Point out each Plasmodium parasite.
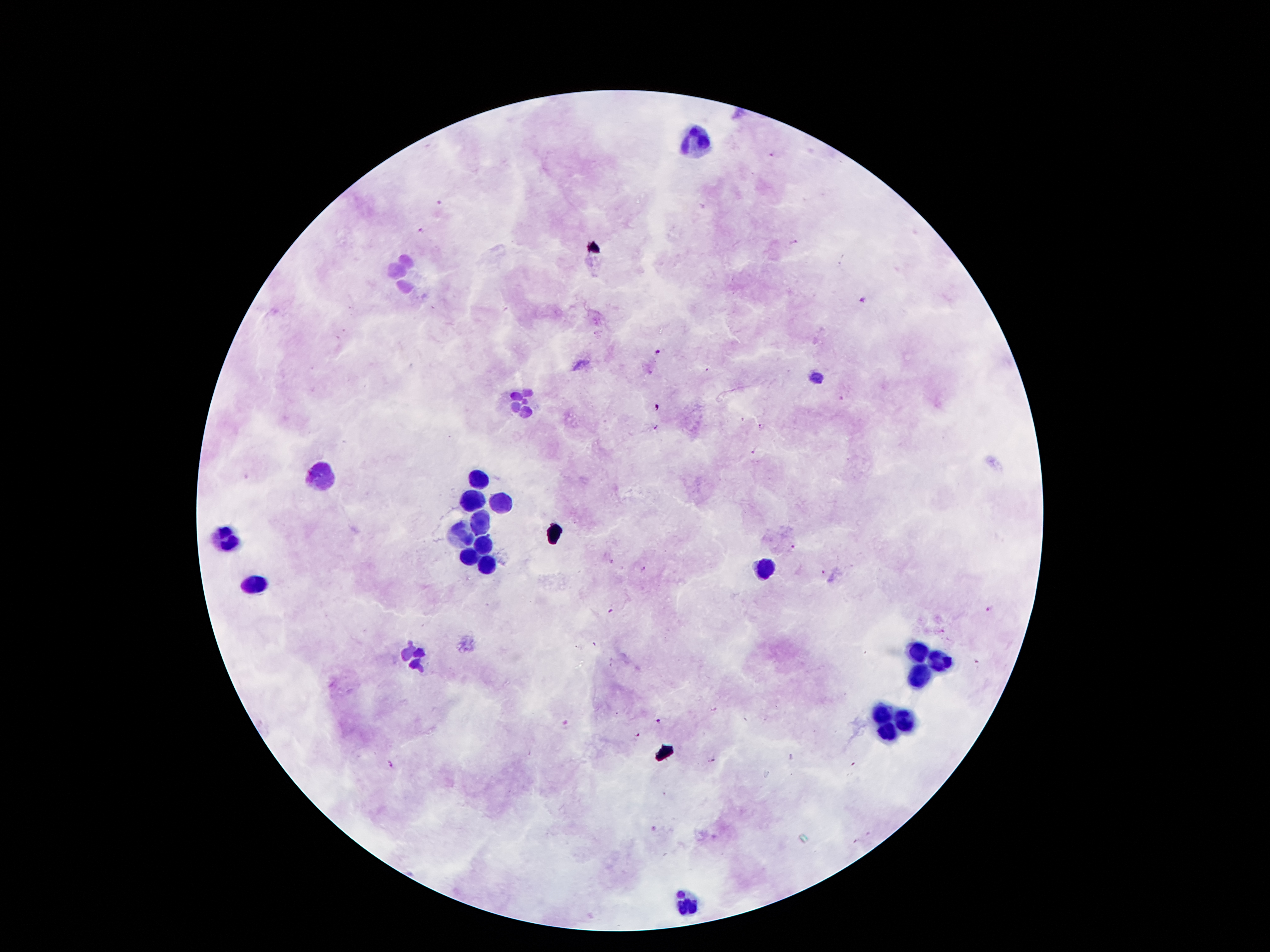

Approximate centers as {x, y} in pixels.
Plasmodium parasites: {772, 156}, {441, 203}, {421, 231}, {794, 242}, {863, 300}, {658, 353}, {843, 398}, {762, 426}, {656, 427}, {755, 451}, {793, 547}, {644, 570}, {825, 573}, {990, 610}, {610, 611}, {713, 709}, {658, 721}, {567, 726}, {636, 735}, {711, 760}, {390, 764}.

Summary:
  - Leukocyte locations: {696, 143}, {404, 276}, {521, 401}, {319, 474}, {478, 476}, {476, 501}, {501, 501}, {480, 520}, {463, 535}, {228, 540}, {478, 545}, {469, 554}, {488, 567}, {764, 567}, {253, 586}, {917, 653}, {415, 658}, {941, 660}, {917, 676}, {882, 713}, {905, 722}, {887, 729}, {687, 901}
  - Patient malaria status: infected with Plasmodium falciparum
  - Capture: smartphone through the microscope eyepiece
  - Preparation: thick peripheral-blood smear
  - Image size: 1270×952 pixels
  - Magnification: 100x
  - Stain: Giemsa
  - Field of view: single